Locate every Plasmodium parasite.
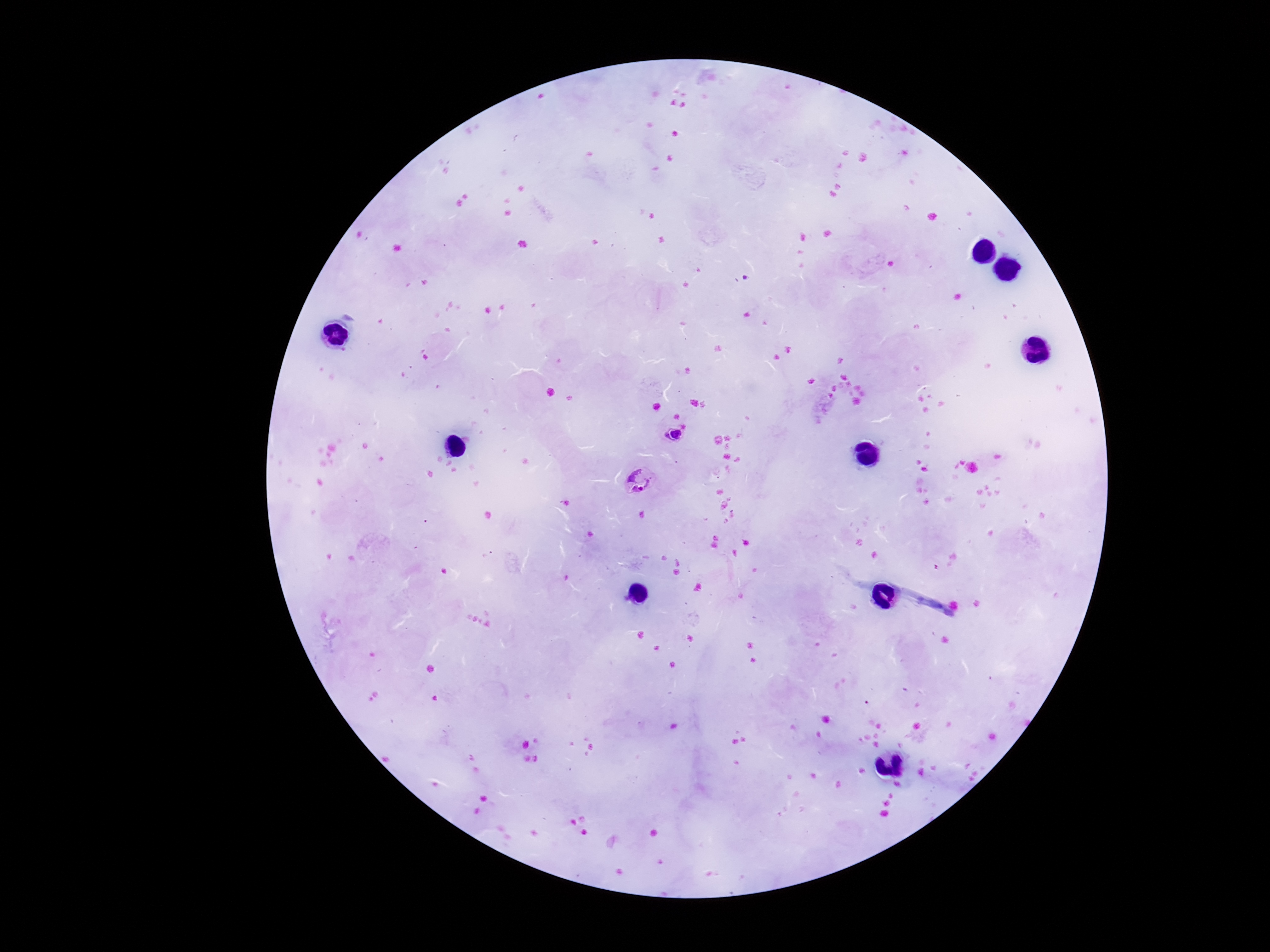

Approximate centers as (x, y) in pixels.
Plasmodium parasites: (673, 435), (640, 481).

stain = Giemsa
field of view = one from this slide
image size = 1270×952 pixels
preparation = thick peripheral-blood smear
capture = smartphone camera through the microscope eyepiece
magnification = 100x
patient malaria status = infected